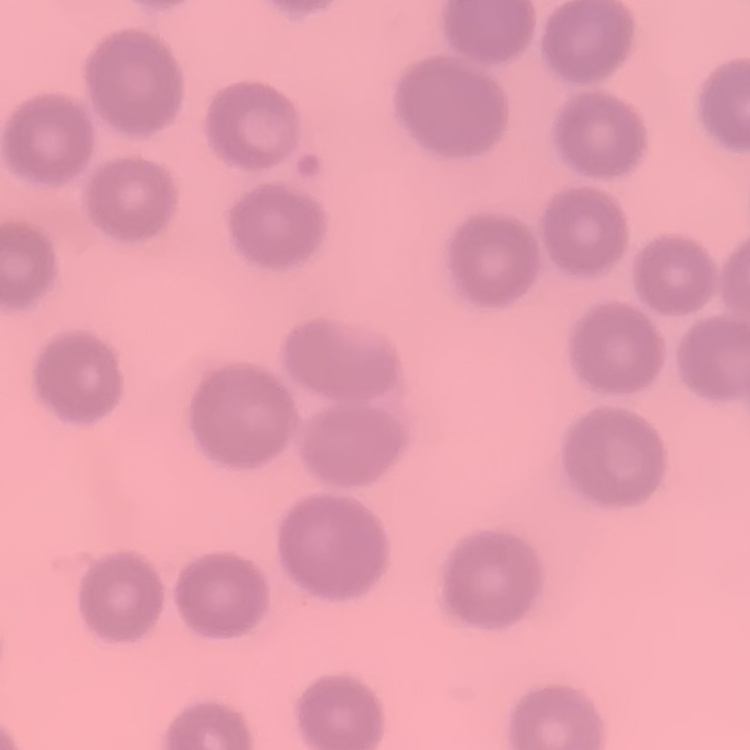 The red blood cells show no rouleaux formation. One tile cut from a larger photomicrograph. Stained with either Field's or Giemsa. Thin peripheral smear.